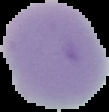
preparation: thin blood film
malaria_status: uninfected
image_size: 109×112 pixels
image_type: segmented cell region on a black background